Assess this cell for malaria.
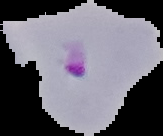
Parasitized.

image type = segmented cell region on a black background
preparation = thin blood smear
image size = 163×136 pixels